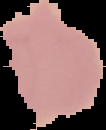

Summary:
  - Image size: 106×130 pixels
  - Result: Plasmodium parasites identified
  - Image type: segmented cell region with the area outside set to black
  - Preparation: thin blood smear